Identify the preparation type.
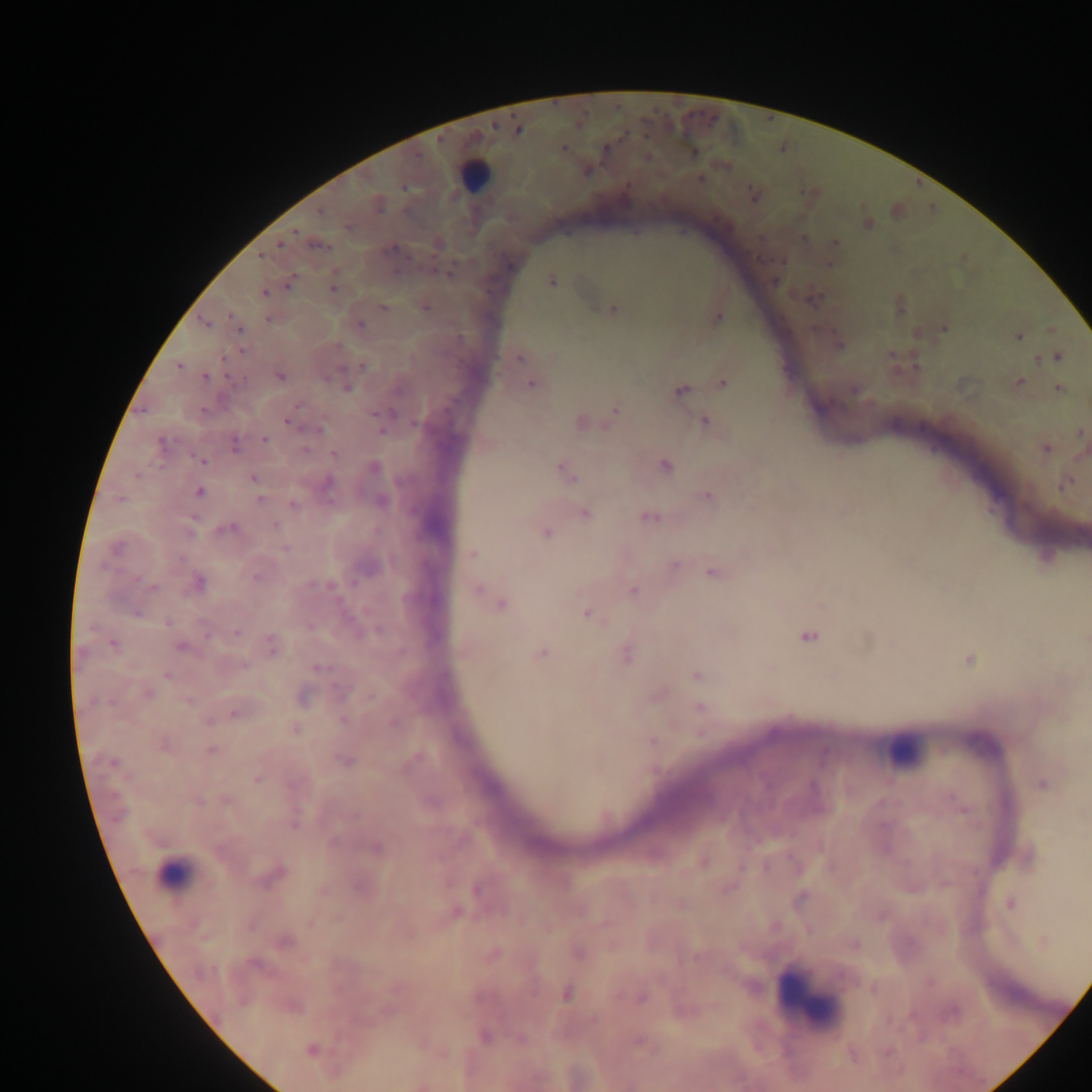

Thick blood smear.

leukocyte locations = approximate centers as (x, y) in pixels: (478, 175), (898, 749), (178, 874), (804, 986)
country = Ghana
capture = mobile-phone photograph through a microscope
image size = 1092×1092 pixels
malaria parasite locations = approximate centers as (x, y) in pixels: (691, 115), (713, 118), (646, 136), (565, 147), (695, 152), (703, 176), (404, 188), (750, 188), (803, 192), (319, 211), (295, 232), (277, 243), (395, 249), (262, 258), (784, 262), (828, 266), (431, 269), (293, 278), (551, 280), (332, 289), (265, 292), (815, 298), (383, 308), (426, 308), (612, 309), (360, 324), (943, 326), (1018, 337), (518, 359), (362, 365), (279, 375), (206, 377), (723, 384), (530, 385), (345, 387), (679, 390), (298, 407), (372, 414), (288, 420), (413, 421), (704, 421), (295, 425), (305, 429), (380, 432), (264, 439), (162, 443), (305, 448), (1045, 450), (333, 453), (201, 461), (664, 466), (252, 479), (1064, 484), (199, 491), (706, 496), (258, 499), (293, 503), (648, 518), (275, 525), (232, 526), (546, 533), (113, 548), (284, 551), (471, 554), (674, 565), (711, 573), (257, 578), (138, 579), (152, 588), (477, 589), (633, 591), (499, 605), (138, 611), (586, 614), (167, 623), (236, 632), (807, 636), (111, 645), (541, 653), (969, 660), (318, 669), (694, 673), (167, 675), (370, 696), (111, 702), (698, 706), (232, 713), (343, 719), (294, 730), (651, 741), (164, 745), (210, 750), (111, 761), (344, 761), (258, 780), (226, 801), (198, 802), (293, 824), (566, 994)
field of view = single